Report the malaria status of this cell.
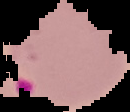

It is parasitized.

image size = 130×112 pixels
preparation = thin blood film
image type = segmented cell region with the area outside set to black